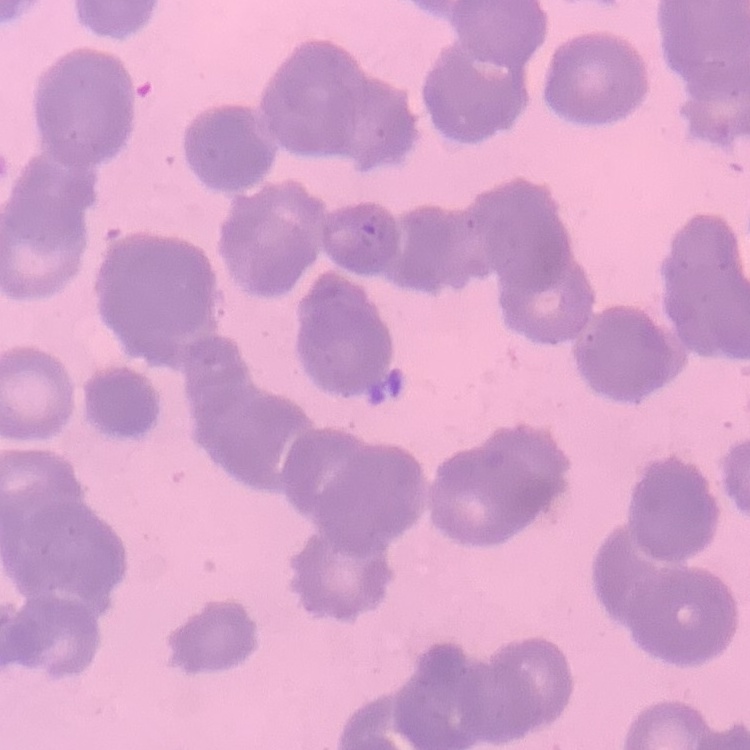 The erythrocytes exhibit rouleaux formation. Field's or Giemsa stain. Square crop of a larger photomicrograph. Thin blood smear.